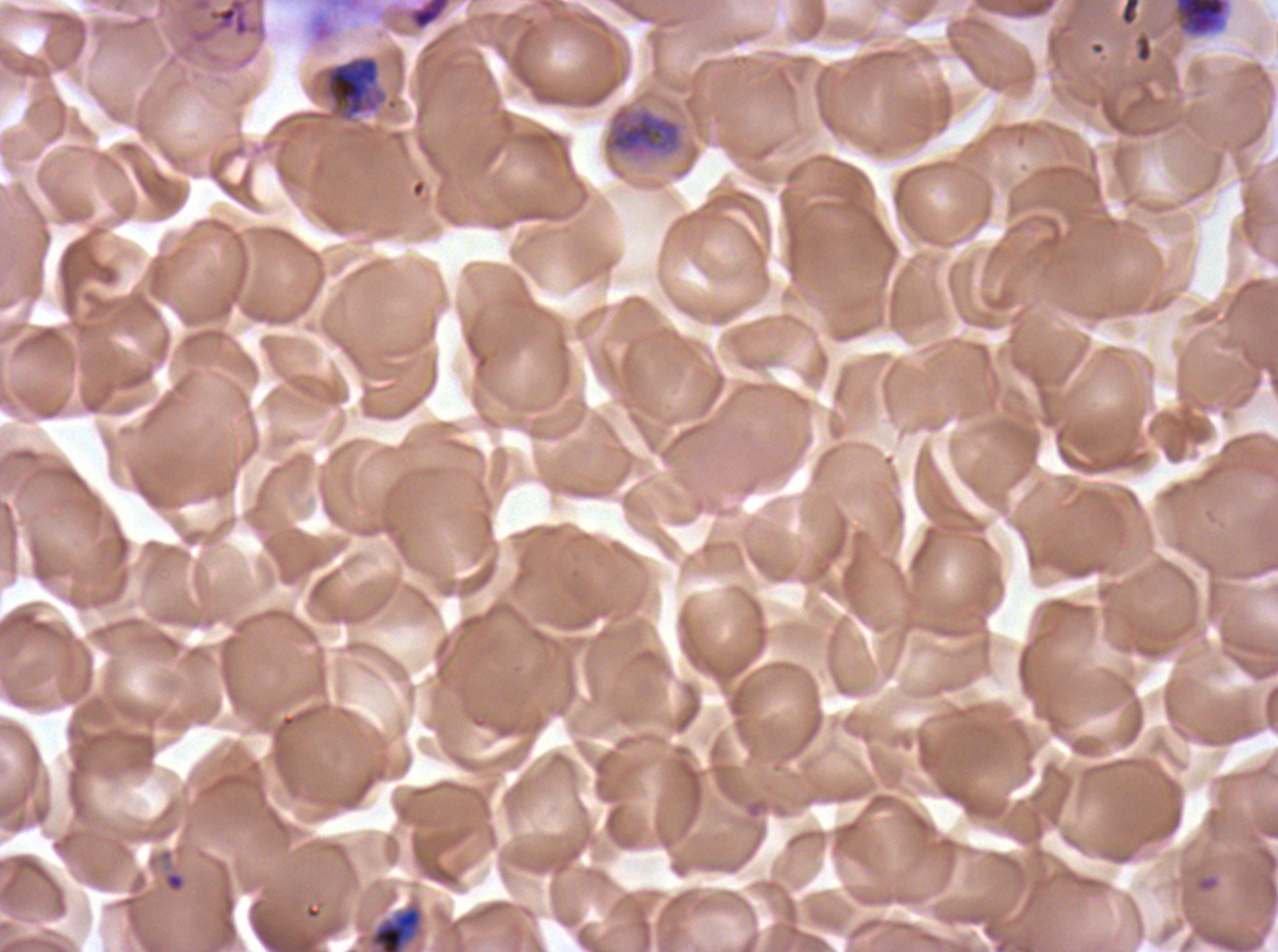
Approximate bounding boxes as {x1, y1, x2, y2} in pixels.
Summary:
  - Ring locations: {146, 848, 189, 895}, {1196, 874, 1220, 893}
  - Debris locations: {403, 0, 453, 32}, {1121, 0, 1140, 25}, {1171, 0, 1232, 39}, {322, 55, 387, 123}, {601, 103, 687, 165}
  - Late trophozoite locations: {368, 904, 424, 951}
  - Image size: 1278×952 pixels
  - Specimen: P. falciparum cultured ex vivo for 24 to 48 hours, from a patient in The Gambia
  - Stain: Giemsa
  - Life-cycle stages observed: ring, late trophozoite
  - Field of view: sub-image separated from a larger composite
  - Preparation: thin blood film